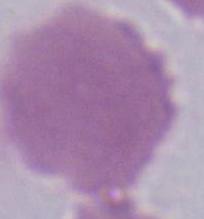 A red blood cell is shown. Captured at 1000x magnification. Photomicrograph.